Locate every Plasmodium parasite.
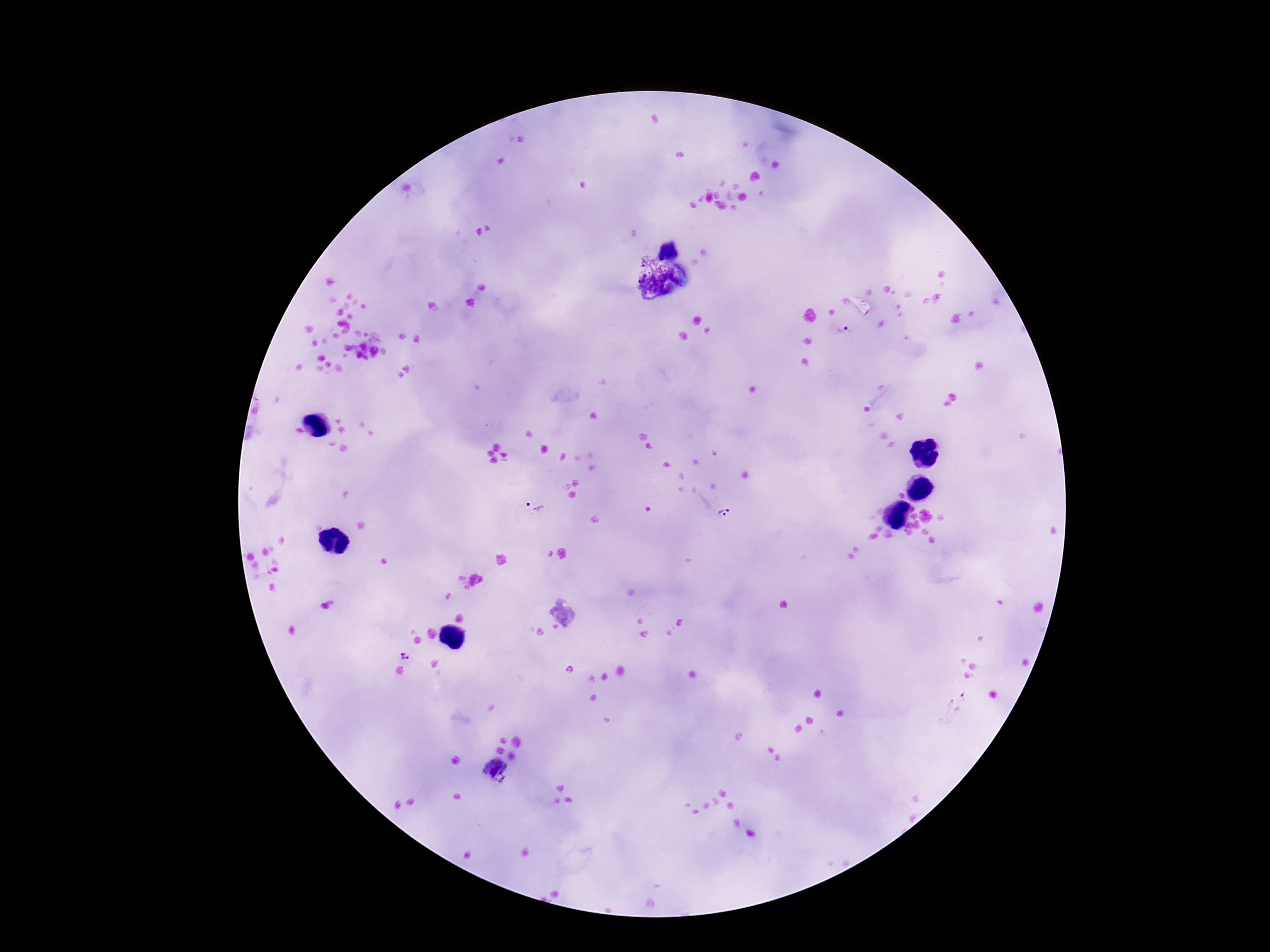
Approximate centers as (x, y) in pixels.
Plasmodium parasites: (844, 331), (535, 505), (724, 513), (406, 655), (494, 772).

Summary:
  - Magnification: 100x
  - Patient malaria status: infected
  - Capture: smartphone camera through the microscope eyepiece
  - Image size: 1270×952 pixels
  - Preparation: thick blood film
  - Stain: Giemsa
  - Field of view: one from this slide